Name the blood parasite species.
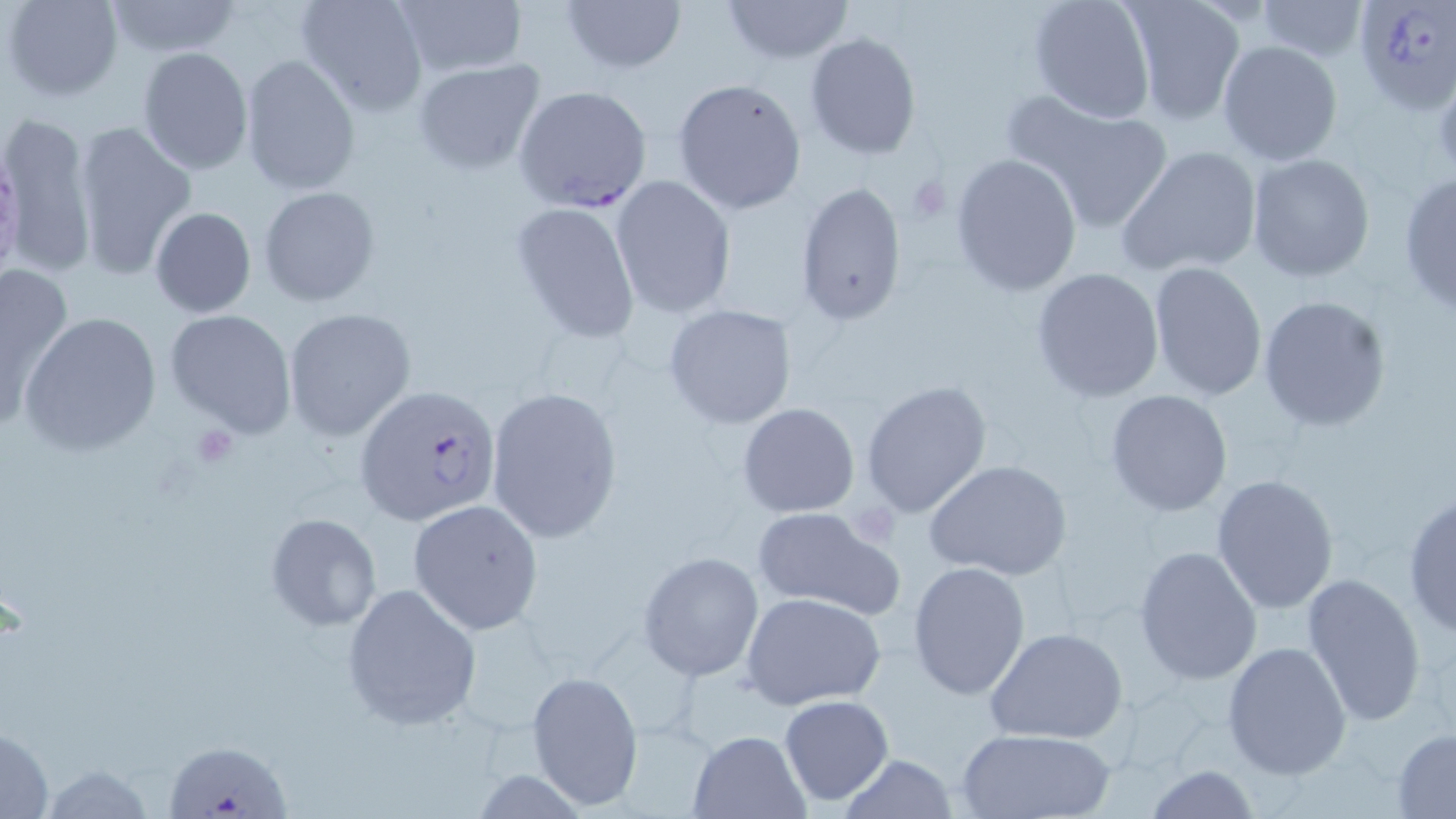
Plasmodium falciparum.

Summary:
  - Coordinate format: approximate bounding boxes as (x1,y1)-(x2,y2) corner pairs in pixels
  - Uninfected red blood cell locations: (5,0)-(124,104), (295,0)-(429,117), (561,0)-(689,75), (720,0)-(855,64), (1026,0)-(1158,124), (101,1)-(244,58), (391,1)-(529,79), (1254,1)-(1370,63), (1120,2)-(1244,126), (804,32)-(921,159), (1217,40)-(1342,166), (137,46)-(253,174), (239,54)-(360,194), (411,58)-(547,175), (671,78)-(808,215), (1009,90)-(1175,234), (2,112)-(97,280), (72,120)-(197,280), (1115,145)-(1262,277), (950,152)-(1081,295), (1247,154)-(1375,283), (1398,168)-(1456,313), (613,179)-(739,324), (796,181)-(910,326), (260,186)-(381,308), (509,201)-(641,342), (150,207)-(256,317), (0,260)-(76,420), (1147,260)-(1268,401), (1031,267)-(1165,402), (1258,294)-(1392,430), (662,303)-(799,431), (283,307)-(416,441), (165,309)-(296,437), (21,311)-(162,454), (860,379)-(993,518), (486,385)-(623,544), (1103,389)-(1234,517), (736,403)-(861,518), (924,459)-(1072,582), (1211,474)-(1340,615), (1402,490)-(1456,636), (408,500)-(546,635), (749,506)-(905,620), (265,513)-(382,631), (1133,545)-(1262,686), (638,550)-(764,681), (907,560)-(1031,699), (1301,572)-(1428,725), (340,581)-(481,730), (742,592)-(885,712), (984,626)-(1128,745), (1222,639)-(1352,780), (526,668)-(645,811), (778,696)-(894,806), (0,724)-(54,819), (954,728)-(1116,818), (687,729)-(809,817), (1391,730)-(1456,816), (836,756)-(961,818), (1145,765)-(1261,819)
  - Platelet locations: (1432,67)-(1456,176), (906,173)-(955,224), (187,424)-(241,469)
  - Plasmodium falciparum-infected red blood cell locations: (1354,0)-(1456,111), (514,85)-(655,215), (354,384)-(504,529), (164,748)-(291,819)
  - Magnification: 1000x
  - Field of view: one of a larger specimen
  - Stain: May-Grünwald-Giemsa
  - Modality: optical microscopy
  - Preparation: thin blood film
  - Image size: 1456×819 pixels